Name the parasite shown.
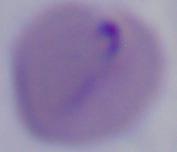

This is Babesia.

Captured at 1000x magnification. Micrograph.